Assess this cell for malaria.
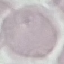
It is uninfected.

Summary:
  - Stain: Giemsa
  - Preparation: thin blood film
  - Capture: smartphone camera at the microscope eyepiece
  - Image type: cell patch, automatically extracted from a larger field of view and resized to 64 × 64 pixels